Describe the morphology of the erythrocytes.
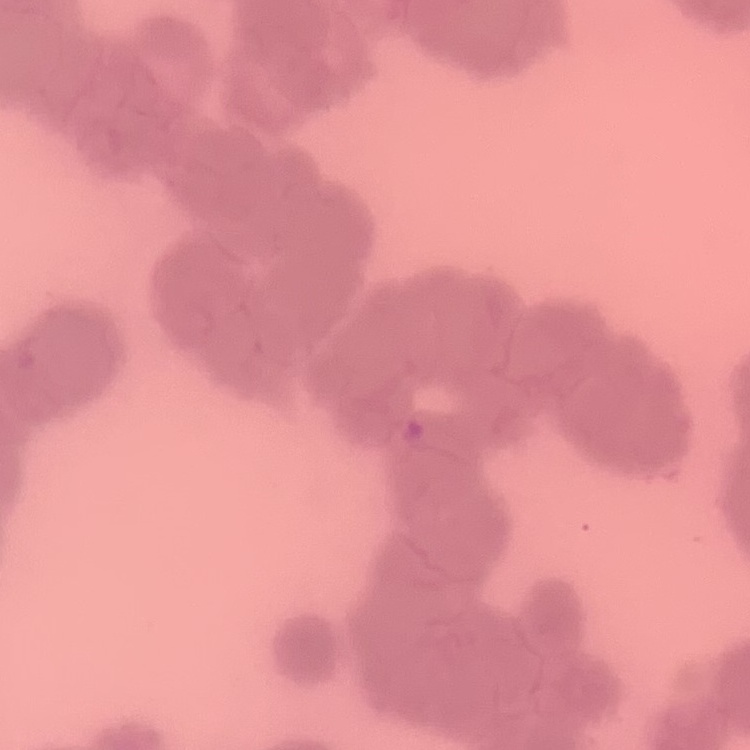

Rouleaux formation.

preparation: thin blood film
image_type: one tile cut from a larger photomicrograph
stain: Field's or Giemsa